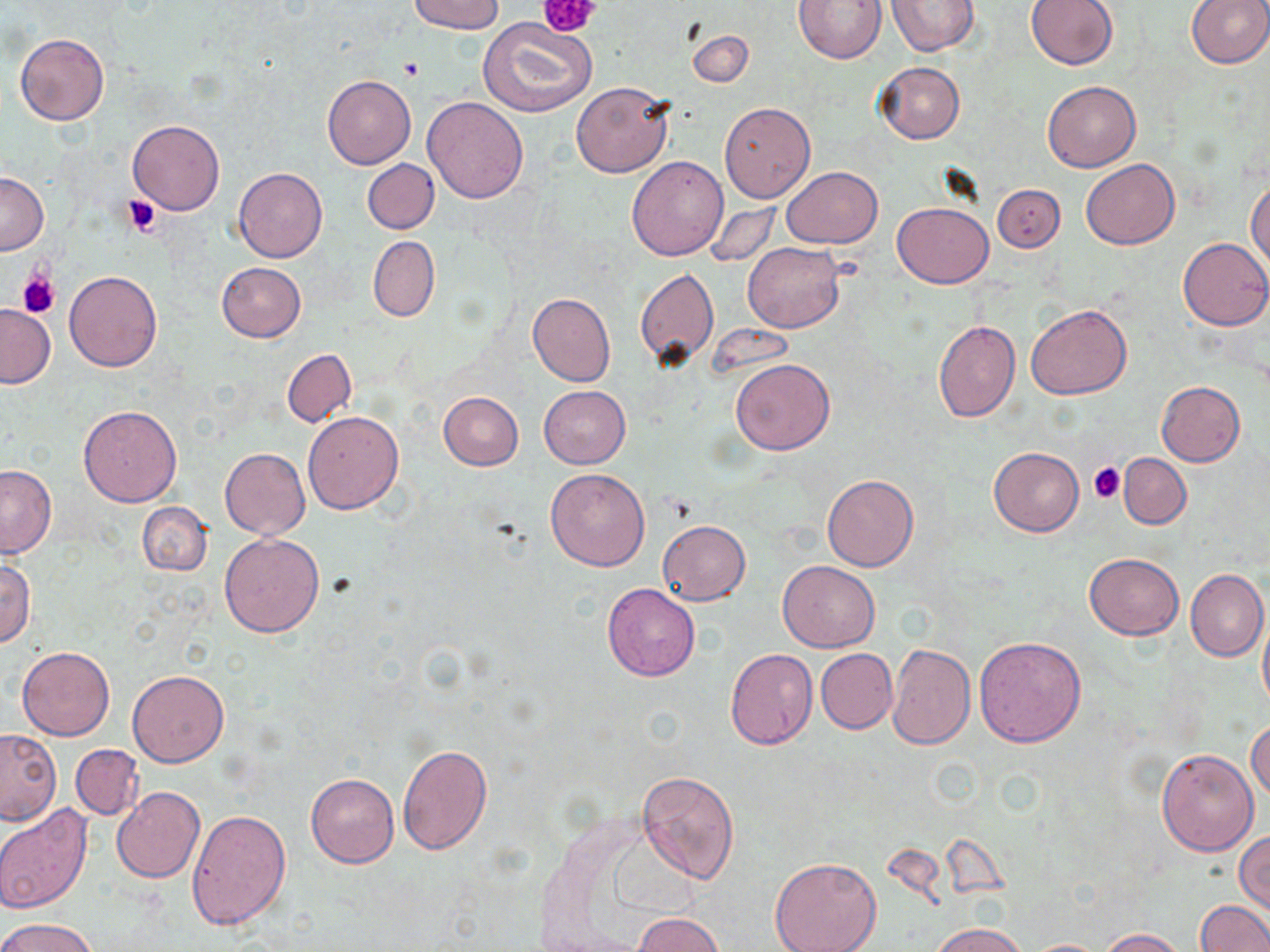

slide-level diagnosis = no evidence of blood parasites
stain = May-Grünwald-Giemsa
field of view = one of a larger specimen
platelet locations = approximate bounding boxes as (x1,y1)-(x2,y2) corner pairs in pixels: (542,0)-(602,38), (398,58)-(426,81), (122,195)-(161,237), (18,273)-(59,318), (1089,462)-(1126,502)
image size = 1270×952 pixels
magnification = 1000x
modality = optical microscopy
uninfected red blood cell locations = approximate bounding boxes as (x1,y1)-(x2,y2) corner pairs in pixels: (409,0)-(505,34), (794,0)-(888,63), (1026,0)-(1119,69), (1185,0)-(1270,68), (886,1)-(980,56), (478,17)-(596,119), (686,31)-(754,88), (15,33)-(109,125), (874,62)-(965,144), (322,75)-(416,169), (1042,81)-(1141,172), (571,82)-(673,177), (423,96)-(529,203), (719,102)-(816,203), (127,120)-(225,215), (626,156)-(728,261), (363,159)-(439,234), (1081,159)-(1179,248), (783,166)-(882,247), (234,168)-(327,262), (0,172)-(48,255), (1247,180)-(1270,270), (993,184)-(1065,252), (892,201)-(993,288), (704,203)-(779,267), (368,236)-(440,322), (1177,238)-(1270,331), (741,243)-(844,333), (215,262)-(305,343), (65,269)-(162,372), (635,269)-(718,367), (528,293)-(616,386), (1026,303)-(1131,400), (0,305)-(54,387), (932,319)-(1021,423), (282,349)-(356,427), (730,359)-(834,455), (1155,381)-(1246,466), (538,386)-(631,468), (438,392)-(523,470), (78,405)-(182,506), (303,411)-(404,515), (987,446)-(1084,537), (219,448)-(309,538), (1120,453)-(1191,528), (0,465)-(56,559), (545,468)-(651,571), (820,473)-(919,571), (137,501)-(211,576), (657,520)-(750,604), (219,532)-(325,638), (1084,553)-(1184,640), (0,558)-(35,648), (778,560)-(880,652), (1185,568)-(1268,662), (602,583)-(700,681), (1259,609)-(1270,715), (974,636)-(1086,747), (886,643)-(975,749), (17,646)-(115,741), (724,649)-(818,750), (815,649)-(897,734), (127,670)-(229,767), (1247,718)-(1270,803), (0,729)-(61,825), (397,742)-(492,855), (70,744)-(143,820), (1156,748)-(1258,855), (637,770)-(740,884), (305,774)-(399,868), (112,786)-(205,884), (0,803)-(93,913), (187,810)-(291,930), (1235,830)-(1270,914), (768,855)-(882,952), (1195,899)-(1269,952), (633,913)-(722,952), (1,917)-(97,952), (931,922)-(1028,952), (1100,928)-(1188,951), (1024,939)-(1113,951)
preparation = thin blood smear